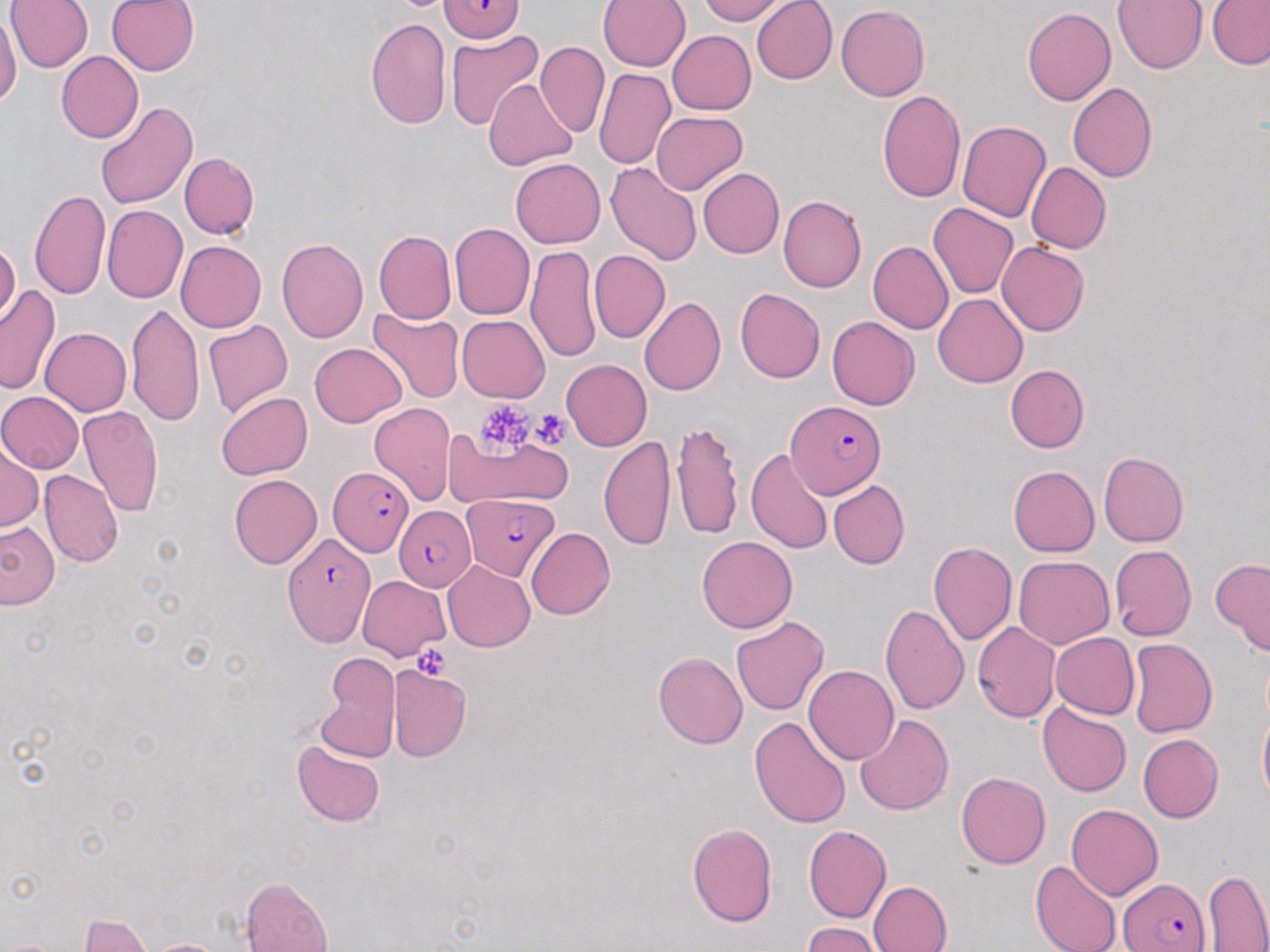
Summary:
  - Coordinate format: approximate bounding boxes as (x1, y1, x2, y2) in pixels
  - Plasmodium falciparum-infected red blood cell locations: (439, 0, 525, 43), (785, 401, 887, 497), (328, 468, 409, 558), (462, 494, 560, 580), (394, 506, 476, 590), (281, 538, 375, 645), (1120, 877, 1210, 952)
  - Uninfected red blood cell locations: (5, 0, 94, 72), (106, 0, 200, 76), (697, 0, 784, 24), (752, 0, 838, 84), (1112, 0, 1209, 74), (598, 1, 690, 72), (1207, 2, 1270, 69), (836, 5, 930, 100), (1021, 8, 1115, 106), (0, 11, 20, 112), (365, 17, 451, 130), (445, 30, 545, 130), (667, 30, 756, 115), (536, 42, 609, 138), (56, 51, 143, 144), (593, 68, 676, 169), (484, 79, 577, 170), (1068, 82, 1158, 182), (877, 88, 967, 203), (95, 103, 197, 209), (652, 111, 748, 195), (957, 121, 1050, 222), (178, 152, 258, 240), (511, 158, 605, 247), (605, 162, 704, 266), (1026, 162, 1110, 254), (698, 168, 784, 258), (30, 190, 109, 301), (778, 195, 866, 292), (929, 203, 1018, 300), (101, 204, 187, 303), (449, 222, 535, 320), (374, 230, 457, 324), (276, 238, 368, 343), (0, 240, 20, 327), (175, 240, 266, 332), (868, 241, 953, 336), (997, 242, 1090, 337), (526, 247, 602, 363), (588, 249, 670, 345), (0, 285, 60, 395), (735, 287, 825, 383), (933, 293, 1028, 388), (639, 297, 726, 397), (127, 304, 203, 429), (368, 310, 465, 405), (457, 315, 549, 403), (827, 315, 920, 410), (203, 321, 294, 419), (40, 328, 132, 416), (310, 342, 407, 427), (561, 359, 652, 451), (1005, 364, 1088, 453), (0, 391, 84, 473), (216, 392, 313, 480), (369, 402, 456, 505), (78, 405, 163, 521), (670, 420, 743, 541), (441, 426, 574, 510), (599, 435, 676, 551), (0, 443, 42, 533), (746, 448, 833, 554), (1098, 452, 1189, 547), (1009, 466, 1099, 557), (40, 469, 124, 567), (228, 473, 321, 569), (828, 480, 909, 570), (0, 521, 59, 609), (526, 527, 615, 620), (696, 535, 798, 633), (928, 542, 1018, 644), (1110, 545, 1196, 641), (1012, 556, 1114, 649), (1210, 558, 1270, 656), (442, 560, 535, 652), (355, 575, 450, 661), (880, 603, 970, 717), (731, 616, 829, 715), (972, 622, 1060, 722), (1050, 632, 1139, 719), (1127, 638, 1216, 737), (653, 650, 747, 749), (315, 653, 401, 764), (386, 664, 472, 762), (803, 665, 899, 766), (1038, 704, 1131, 798), (1257, 706, 1270, 812), (854, 713, 953, 816), (749, 717, 850, 829), (1137, 733, 1223, 822), (291, 740, 385, 827), (956, 772, 1051, 869), (1067, 805, 1163, 900), (687, 823, 778, 927), (803, 824, 891, 924), (1031, 860, 1121, 952), (1202, 869, 1270, 950), (241, 877, 334, 952), (868, 880, 953, 952), (80, 914, 151, 951), (801, 923, 882, 952), (144, 938, 233, 951), (0, 940, 64, 952)
  - Platelet locations: (472, 402, 545, 452), (529, 410, 572, 448), (413, 644, 455, 678)
  - Slide-level diagnosis: Plasmodium falciparum
  - Stain: May-Grünwald-Giemsa
  - Preparation: thin blood smear
  - Modality: optical microscopy
  - Field of view: one of a larger specimen
  - Magnification: 1000x
  - Image size: 1270×952 pixels